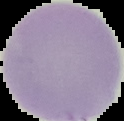

Summary:
  - Image size: 124×121 pixels
  - Image type: cell region segmented out of the field of view; surrounding area masked to black
  - Preparation: thin blood smear
  - Malaria status: uninfected